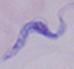

A trypanosome is seen. Micrograph. 1000x magnification.